Assess this cell for malaria.
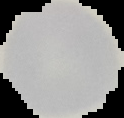

Uninfected.

image size = 124×118 pixels
preparation = thin blood film
image type = cell region segmented out of the field of view; surrounding area masked to black